Give the extent of all Trypanosoma brucei.
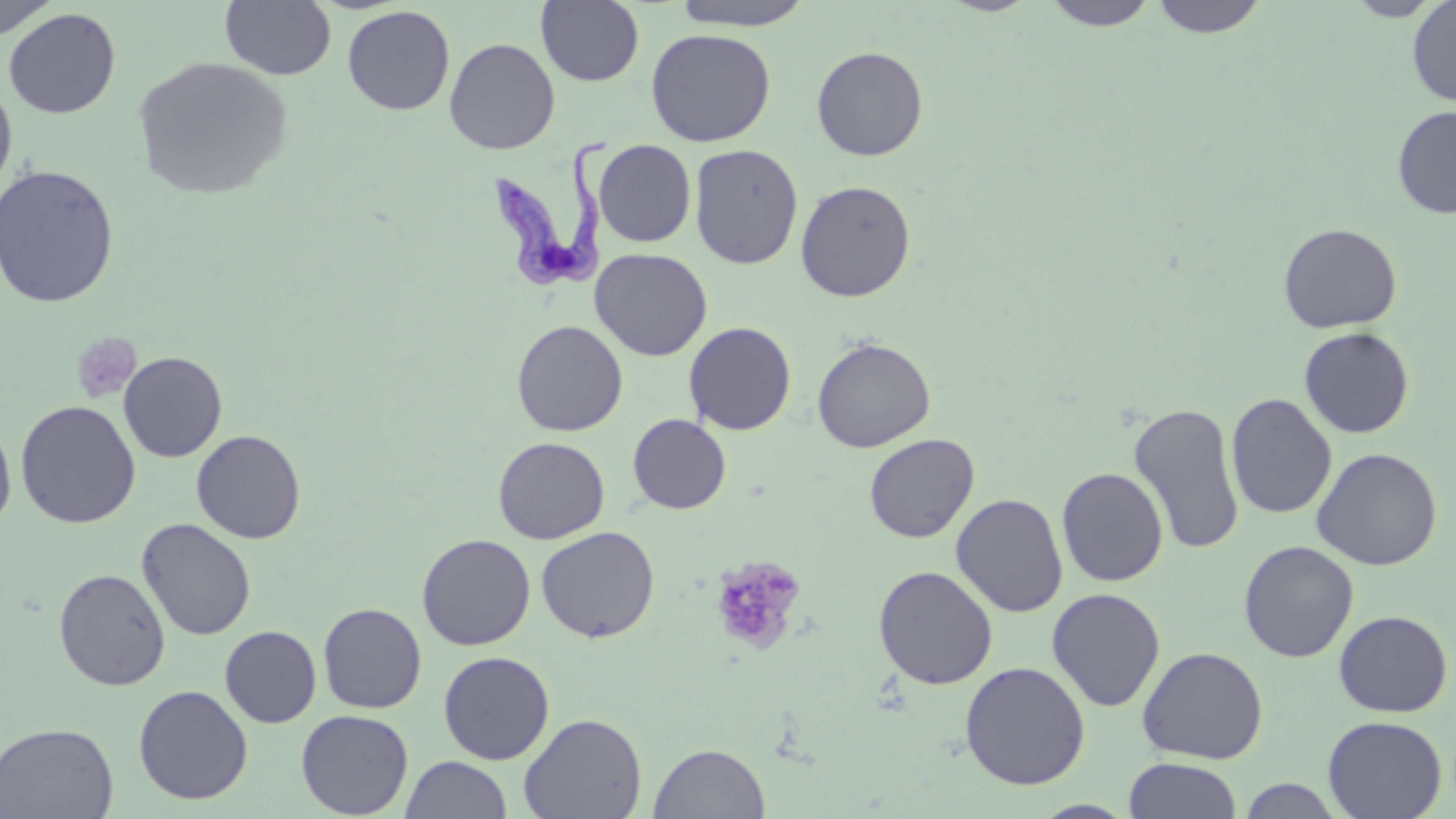

Approximate bounding boxes as (x1, y1, x2, y2) in pixels.
Trypanosoma brucei: (491, 132, 619, 289).

Summary:
  - Platelet locations: (71, 332, 141, 404), (708, 555, 807, 653)
  - Uninfected red blood cell locations: (535, 0, 645, 86), (669, 0, 818, 30), (1041, 0, 1159, 30), (1150, 0, 1269, 38), (1345, 0, 1447, 21), (1407, 0, 1456, 107), (0, 1, 61, 39), (220, 1, 336, 81), (342, 5, 455, 115), (3, 8, 121, 119), (646, 28, 776, 147), (444, 37, 560, 154), (811, 45, 929, 161), (131, 55, 293, 200), (0, 77, 18, 195), (1392, 105, 1456, 219), (593, 139, 696, 247), (689, 143, 803, 270), (0, 164, 120, 309), (795, 179, 916, 302), (1278, 222, 1403, 334), (590, 248, 712, 361), (511, 319, 628, 436), (684, 321, 797, 435), (1299, 327, 1415, 438), (812, 336, 935, 452), (118, 351, 228, 463), (1225, 393, 1338, 520), (15, 400, 141, 528), (1128, 402, 1245, 555), (628, 414, 731, 514), (0, 416, 17, 533), (192, 429, 306, 544), (864, 433, 979, 543), (493, 436, 610, 544), (1311, 447, 1442, 571), (1057, 466, 1169, 587), (951, 493, 1068, 617), (136, 518, 256, 641), (536, 526, 660, 643), (417, 533, 536, 650), (1238, 541, 1359, 663), (873, 565, 998, 689), (54, 568, 171, 691), (1046, 588, 1166, 712), (318, 602, 427, 713), (1334, 610, 1453, 717), (219, 625, 322, 728), (1137, 647, 1268, 764), (438, 650, 555, 764), (959, 661, 1090, 790), (134, 684, 253, 805), (296, 709, 414, 818), (518, 712, 647, 819), (1323, 715, 1448, 819), (0, 721, 118, 818), (648, 742, 770, 818), (401, 756, 512, 818), (1124, 758, 1242, 819), (1235, 777, 1347, 818), (1029, 800, 1138, 818)
  - Slide-level diagnosis: Trypanosoma brucei
  - Magnification: 1000x
  - Preparation: thin blood film
  - Field of view: one of a larger specimen
  - Image size: 1456×819 pixels
  - Modality: light microscopy
  - Stain: May-Grünwald-Giemsa